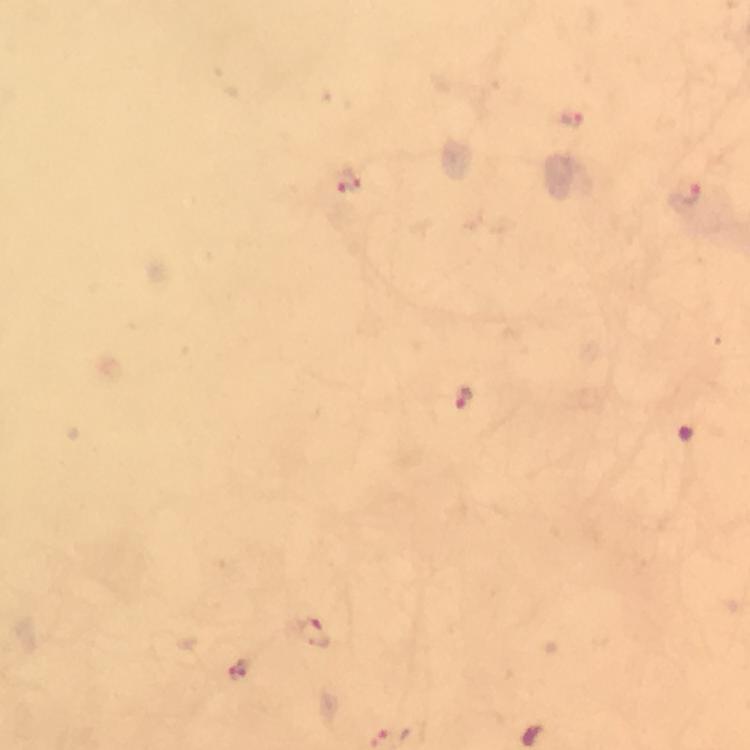
Approximate centers as {x, y} in pixels. Malaria parasite locations: {571, 118}, {347, 181}, {688, 191}, {464, 398}, {314, 632}, {243, 670}. Image is 750×750 pixels. Giemsa-stained preparation. 100x magnification. A crop from one field of view. Thick smear. From a diagnostic examination for malaria. Photographed through the microscope with a smartphone camera. Immersion oil was used.